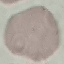
Summary:
  - Malaria status: uninfected
  - Capture: smartphone through the microscope eyepiece
  - Stain: Giemsa
  - Preparation: thin smear
  - Image type: cell patch, automatically extracted from a larger field of view and resized to 64 × 64 pixels